Classify this cell by malaria status.
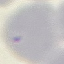

It is uninfected.

preparation = thin smear
stain = Giemsa
capture = smartphone camera at the microscope eyepiece
image type = automatically extracted cell patch, resized to 64 × 64 pixels